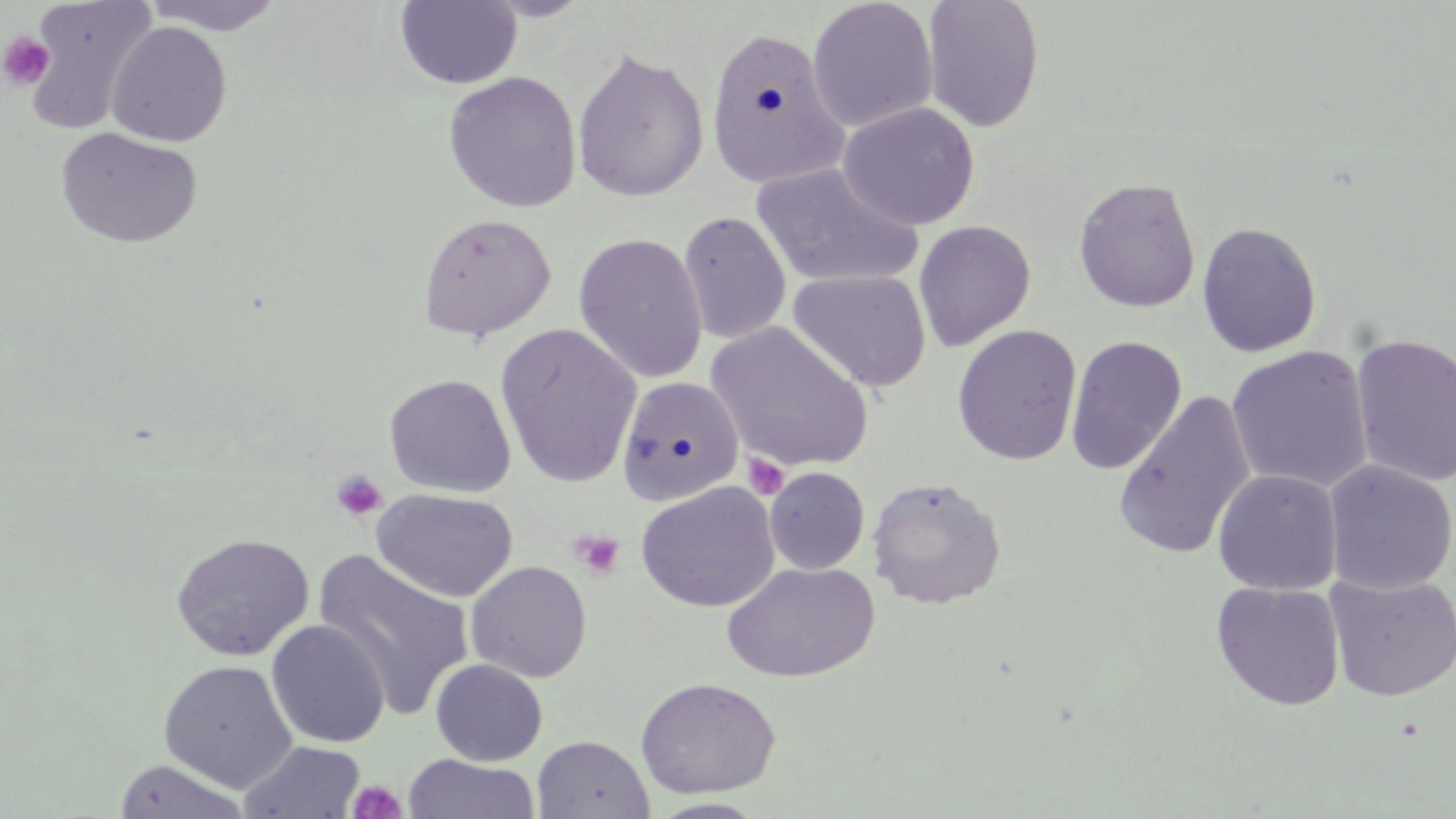
Summary:
  - Coordinate format: approximate bounding boxes as [x1, y1, x2, y2] in pixels
  - Platelet locations: [0, 32, 55, 91], [742, 453, 789, 500], [331, 470, 388, 521], [569, 530, 626, 582], [347, 781, 408, 819]
  - Uninfected red blood cell locations: [23, 0, 159, 134], [140, 0, 290, 36], [806, 0, 939, 133], [921, 0, 1045, 133], [394, 1, 522, 89], [106, 21, 232, 148], [704, 25, 850, 191], [570, 46, 709, 203], [443, 71, 582, 213], [837, 102, 980, 231], [55, 127, 203, 249], [750, 163, 921, 289], [1073, 177, 1201, 313], [677, 211, 792, 345], [417, 212, 556, 341], [914, 220, 1037, 352], [1197, 221, 1322, 358], [572, 231, 708, 384], [788, 269, 931, 394], [706, 321, 874, 473], [495, 323, 642, 488], [951, 324, 1083, 466], [1350, 333, 1456, 489], [1065, 335, 1187, 475], [1225, 345, 1374, 494], [384, 373, 517, 498], [617, 376, 744, 506], [1112, 390, 1257, 560], [1323, 461, 1456, 596], [764, 466, 870, 575], [1212, 469, 1342, 595], [867, 476, 1006, 610], [635, 481, 780, 612], [371, 488, 518, 602], [170, 532, 314, 662], [312, 549, 476, 721], [465, 560, 591, 683], [721, 562, 878, 683], [1325, 573, 1456, 702], [1211, 581, 1345, 711], [266, 619, 390, 748], [158, 659, 298, 792], [430, 659, 548, 766], [635, 677, 781, 798], [532, 735, 654, 819], [238, 740, 366, 819], [403, 754, 539, 819], [111, 758, 254, 819], [646, 798, 771, 818]
  - Slide-level diagnosis: negative for blood parasites
  - Modality: optical microscopy
  - Field of view: single
  - Preparation: thin blood smear
  - Magnification: 1000x
  - Image size: 1456×819 pixels
  - Stain: May-Grünwald-Giemsa